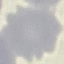

malaria status = uninfected
capture = smartphone camera at the microscope eyepiece
image type = automatically extracted cell patch, resized to 64 × 64 pixels
preparation = thin smear
stain = Giemsa